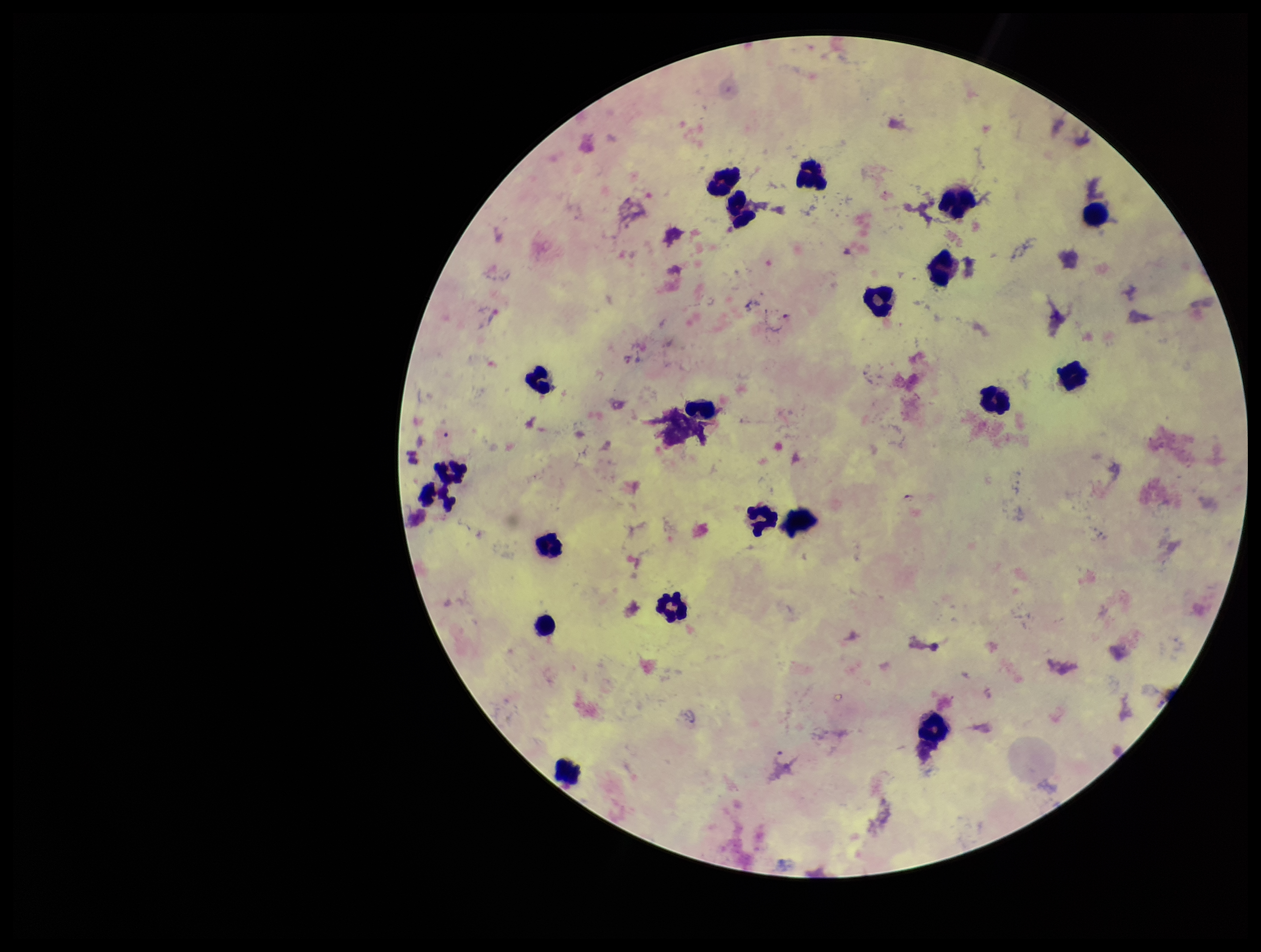

{
  "capture": "smartphone photograph through the microscope eyepiece",
  "image_size": "1261×952 pixels",
  "patient_malaria_status": "infected",
  "plasmodium_parasites": "detected",
  "species_reported_for_this_patient": "Plasmodium falciparum",
  "preparation": "thick blood smear",
  "parasite_count": 1,
  "field_of_view": "one from this slide",
  "leukocyte_count": 20,
  "stain": "Giemsa"
}